Outline each Plasmodium ovale-infected red blood cell.
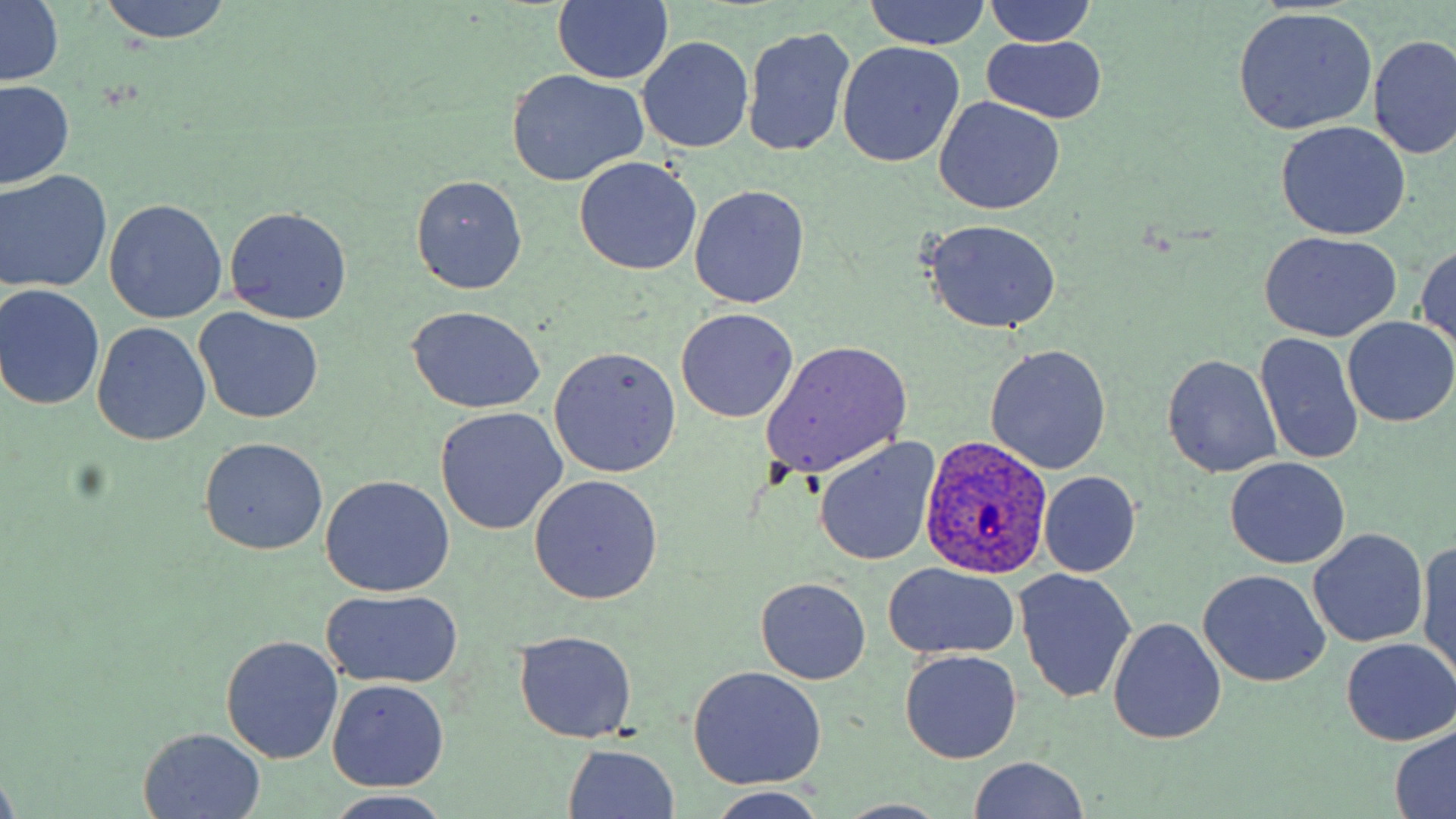

Approximate bounding boxes as [x1, y1, x2, y2] in pixels.
Plasmodium ovale-infected red blood cells: [919, 435, 1053, 579].

Summary:
  - Uninfected red blood cell locations: [97, 0, 233, 44], [863, 0, 991, 51], [552, 1, 673, 86], [984, 1, 1098, 48], [1, 2, 63, 89], [1233, 7, 1377, 135], [744, 24, 855, 158], [1370, 32, 1456, 161], [639, 35, 753, 153], [982, 37, 1108, 123], [837, 42, 965, 167], [505, 70, 649, 186], [0, 81, 74, 189], [935, 97, 1065, 214], [1275, 121, 1410, 241], [575, 157, 701, 275], [1, 170, 112, 293], [411, 174, 527, 293], [691, 186, 810, 309], [105, 198, 227, 324], [225, 206, 352, 325], [921, 218, 1062, 334], [1258, 232, 1401, 343], [1416, 244, 1455, 357], [0, 285, 106, 410], [406, 306, 545, 415], [194, 308, 323, 424], [675, 308, 799, 424], [1344, 319, 1456, 425], [92, 323, 210, 445], [1255, 331, 1365, 468], [761, 339, 913, 479], [984, 343, 1113, 474], [549, 345, 681, 478], [1162, 353, 1283, 478], [434, 407, 567, 536], [199, 437, 328, 554], [815, 439, 938, 565], [1223, 457, 1350, 569], [1039, 472, 1141, 576], [322, 475, 454, 597], [527, 475, 663, 605], [1309, 528, 1428, 647], [1417, 538, 1456, 681], [882, 562, 1021, 661], [1199, 570, 1331, 688], [1016, 571, 1136, 702], [757, 578, 871, 685], [322, 589, 462, 690], [1108, 617, 1226, 745], [514, 631, 638, 743], [221, 634, 343, 765], [1342, 638, 1454, 744], [898, 649, 1023, 764], [688, 665, 827, 790], [326, 678, 453, 792], [1389, 725, 1455, 819], [140, 729, 266, 816], [561, 744, 681, 819], [966, 757, 1092, 818], [0, 772, 22, 819], [706, 791, 831, 819], [834, 800, 950, 818]
  - Slide-level diagnosis: Plasmodium ovale
  - Stain: May-Grünwald-Giemsa
  - Field of view: one of a larger specimen
  - Magnification: 1000x
  - Image size: 1456×819 pixels
  - Preparation: thin blood film
  - Modality: optical microscopy